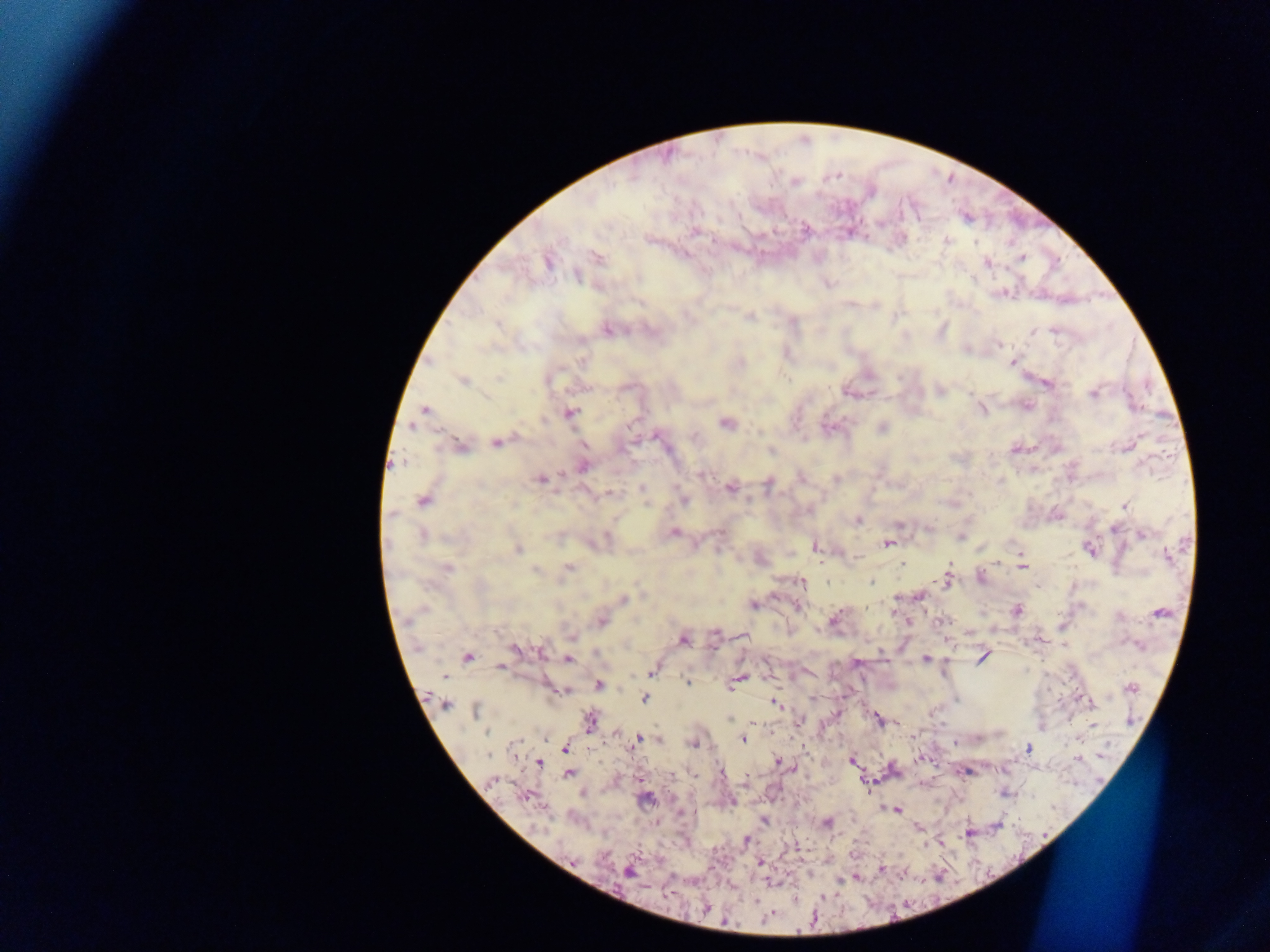

capture = mobile-phone photograph through a microscope
country = Ghana
field of view = single
preparation = thick blood film
image size = 1270×952 pixels
malaria parasite locations = approximate centers as {x, y} in pixels: {834, 177}, {794, 182}, {903, 209}, {804, 230}, {645, 240}, {946, 242}, {976, 242}, {594, 257}, {1020, 258}, {546, 262}, {987, 264}, {828, 284}, {685, 314}, {750, 316}, {796, 326}, {1054, 328}, {606, 329}, {627, 331}, {1046, 331}, {1033, 333}, {997, 346}, {966, 349}, {583, 358}, {429, 362}, {740, 362}, {1011, 362}, {462, 380}, {1049, 384}, {941, 391}, {621, 392}, {1092, 392}, {843, 393}, {980, 408}, {425, 409}, {569, 413}, {543, 421}, {726, 424}, {882, 426}, {655, 432}, {759, 432}, {657, 436}, {694, 436}, {494, 442}, {460, 445}, {1124, 448}, {771, 451}, {396, 465}, {702, 474}, {563, 475}, {800, 477}, {834, 479}, {540, 480}, {998, 481}, {768, 484}, {729, 487}, {642, 488}, {609, 493}, {421, 501}, {683, 501}, {646, 504}, {1124, 505}, {393, 512}, {859, 521}, {897, 525}, {1113, 529}, {673, 532}, {718, 533}, {1143, 534}, {424, 535}, {553, 536}, {606, 537}, {962, 538}, {885, 545}, {814, 549}, {518, 550}, {1016, 550}, {1089, 551}, {719, 552}, {854, 559}, {900, 565}, {949, 565}, {1022, 566}, {449, 568}, {569, 568}, {535, 569}, {981, 576}, {947, 579}, {801, 581}, {870, 582}, {562, 583}, {828, 583}, {919, 598}, {623, 599}, {895, 600}, {754, 604}, {799, 608}, {1018, 611}, {1160, 613}, {835, 616}, {601, 620}, {575, 635}, {713, 638}, {683, 639}, {1065, 646}, {511, 647}, {539, 653}, {598, 653}, {980, 657}, {468, 658}, {926, 658}, {568, 659}, {501, 668}, {652, 672}, {443, 676}, {743, 677}, {686, 682}, {598, 683}, {734, 683}, {547, 685}, {1131, 687}, {567, 690}, {562, 693}, {815, 696}, {645, 698}, {775, 704}, {446, 706}, {476, 709}, {876, 717}, {729, 719}, {800, 720}, {589, 721}, {880, 722}, {756, 724}, {1092, 725}, {487, 733}, {542, 738}, {638, 739}, {659, 741}, {742, 741}, {635, 742}, {957, 742}, {515, 744}, {695, 744}, {565, 748}, {1027, 749}, {489, 755}, {852, 760}, {1075, 760}, {777, 761}, {539, 762}, {722, 773}, {969, 773}, {568, 774}, {492, 781}, {1003, 794}, {888, 809}, {898, 811}, {683, 814}, {765, 821}, {828, 822}, {996, 826}, {970, 835}, {746, 839}, {942, 842}, {759, 862}, {881, 869}, {627, 873}, {840, 882}, {756, 903}